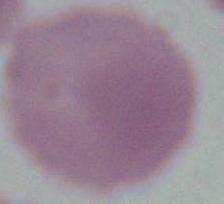

magnification = 1000x
identification = red blood cell
modality = photomicrograph